Assess this cell for malaria.
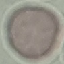
It is uninfected.

{
  "stain": "Giemsa",
  "capture": "smartphone through the microscope eyepiece",
  "preparation": "thin blood smear",
  "image_type": "cell patch, automatically extracted from a larger field of view and resized to 64 × 64 pixels"
}